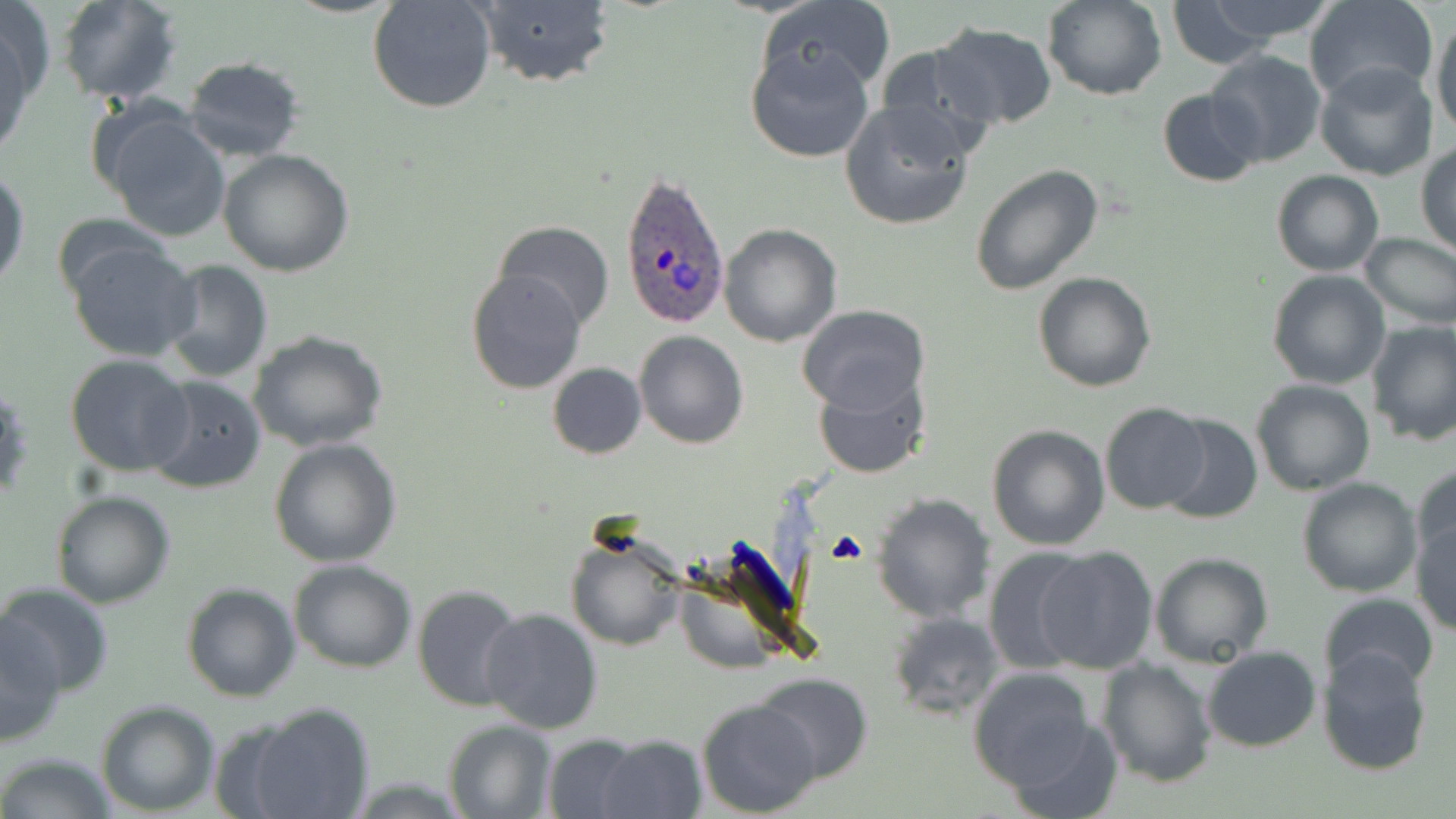
Approximate bounding boxes as [x1, y1, x2, y2] in pixels. Plasmodium ovale-infected red blood cell locations: [618, 172, 731, 333]. Uninfected red blood cell locations: [57, 0, 184, 105], [367, 0, 497, 115], [1043, 0, 1166, 100], [1303, 0, 1438, 103], [758, 1, 897, 100], [1151, 1, 1319, 62], [469, 2, 616, 89], [0, 3, 50, 140], [1429, 11, 1456, 138], [928, 23, 1057, 129], [744, 40, 877, 162], [873, 44, 998, 161], [1206, 49, 1326, 168], [181, 56, 306, 162], [1315, 61, 1440, 182], [1158, 87, 1265, 187], [839, 100, 975, 231], [97, 105, 231, 242], [1416, 145, 1456, 256], [217, 150, 355, 278], [969, 163, 1104, 295], [0, 166, 30, 298], [1270, 170, 1384, 277], [492, 220, 616, 333], [718, 224, 841, 347], [1359, 231, 1456, 332], [66, 239, 199, 362], [158, 259, 275, 384], [466, 267, 588, 395], [1267, 270, 1391, 390], [1032, 272, 1158, 391], [797, 305, 930, 415], [1366, 321, 1456, 446], [246, 328, 387, 453], [633, 330, 749, 449], [65, 353, 195, 476], [546, 362, 647, 459], [813, 368, 930, 480], [143, 375, 268, 493], [1250, 379, 1376, 497], [1100, 402, 1212, 515], [1158, 413, 1262, 524], [986, 424, 1111, 551], [269, 438, 402, 569], [1410, 464, 1456, 575], [1296, 476, 1421, 597], [51, 491, 175, 609], [870, 492, 997, 624], [1411, 515, 1456, 634], [566, 530, 689, 651], [1036, 545, 1158, 675], [982, 546, 1096, 675], [1148, 552, 1274, 667], [288, 559, 417, 672], [180, 581, 302, 702], [0, 582, 114, 699], [411, 583, 526, 713], [1316, 594, 1440, 692], [481, 607, 602, 736], [889, 613, 1007, 721], [1, 617, 67, 745], [1202, 645, 1321, 752], [1317, 648, 1434, 775], [1097, 658, 1218, 789], [968, 668, 1098, 791], [752, 673, 874, 783], [695, 699, 822, 818], [96, 700, 220, 815], [236, 703, 376, 819], [1002, 714, 1125, 819], [443, 719, 556, 818], [542, 733, 645, 817], [595, 735, 709, 819], [0, 751, 118, 818]. Platelet locations: [827, 531, 869, 567]. Slide-level diagnosis: Plasmodium ovale. Single field of view. Thin blood film. 1000x magnification. May-Grünwald-Giemsa-stained preparation. Image is 1456×819 pixels. Optical microscopy.